Look for Plasmodium parasites.
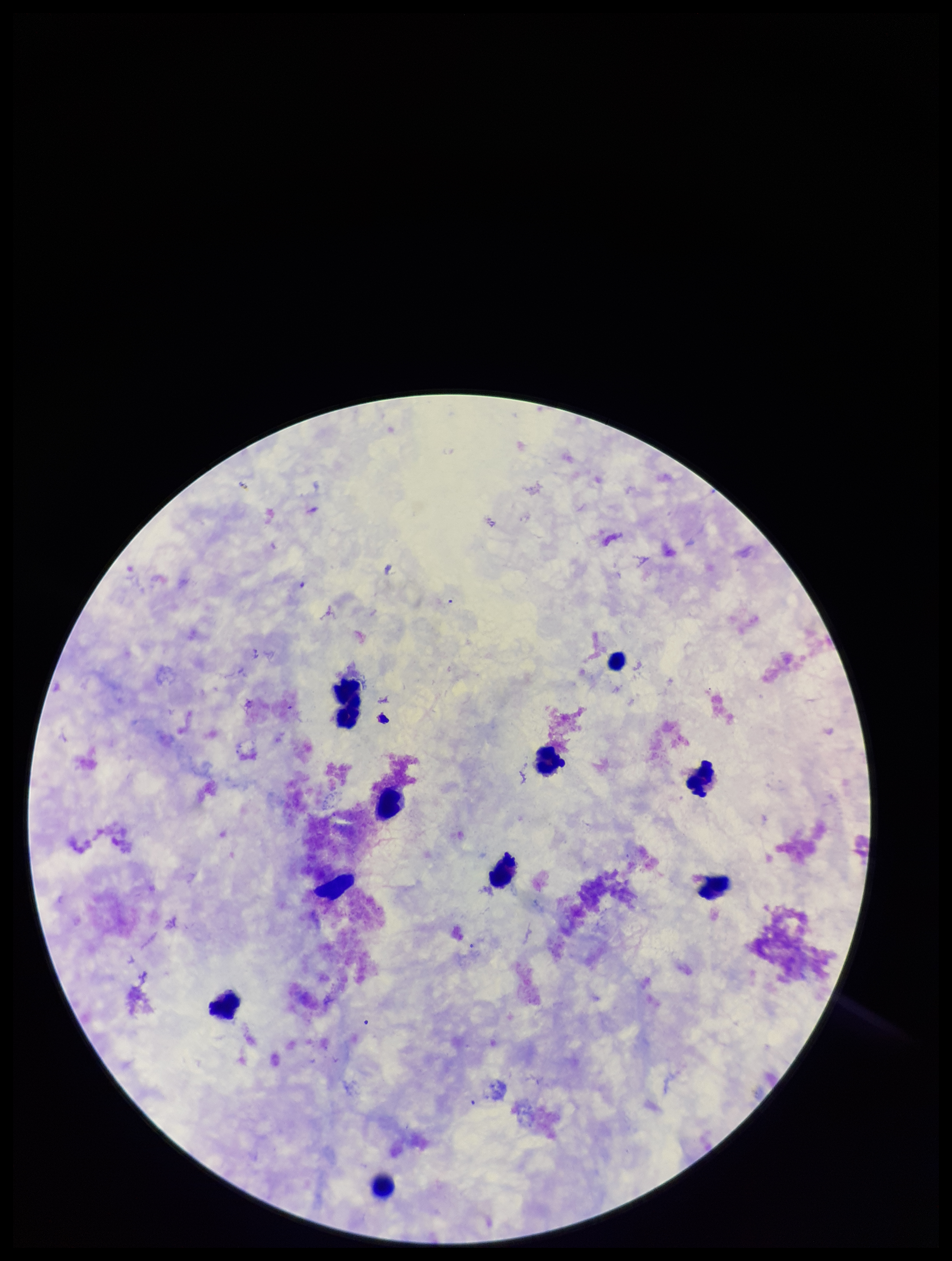

None identified.

field of view = one from this slide
patient malaria status = negative
image size = 952×1261 pixels
stain = Giemsa
parasite count = 0
leukocyte count = 9
capture = smartphone photograph through the microscope eyepiece
preparation = thick smear